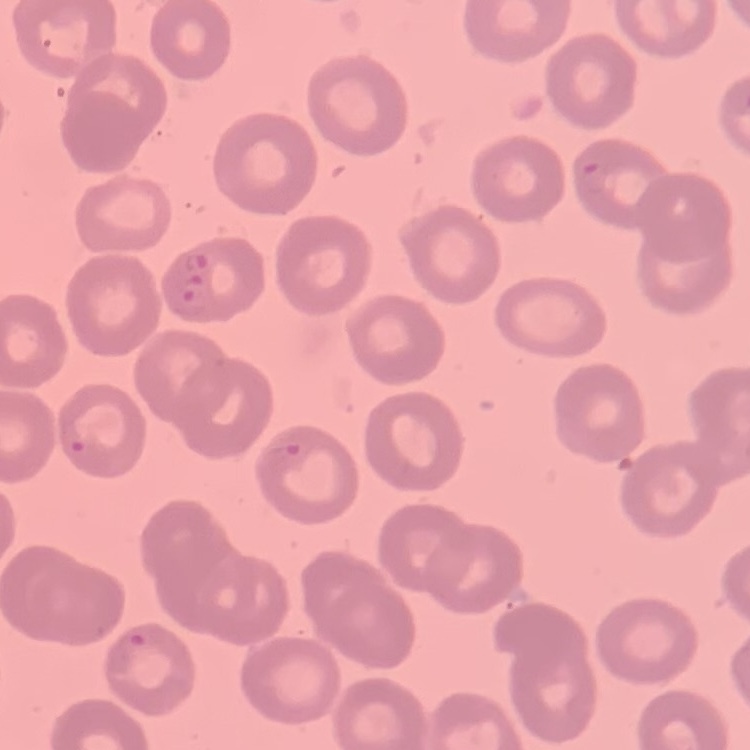
red blood cell morphology = no rouleaux formation
image type = square crop of a larger photomicrograph
preparation = thin blood smear
stain = Field's or Giemsa